Point out each malaria parasite.
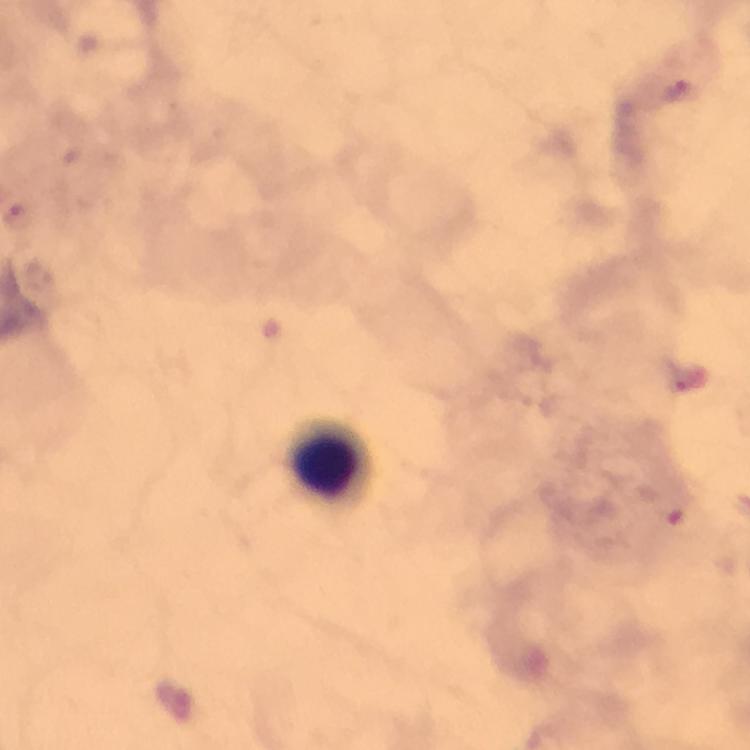

Approximate centers as [x, y] in pixels.
Malaria parasites: [694, 379].

Leukocyte locations: [325, 469]. Immersion oil was used. At 100x magnification. Image is 750×750 pixels. From a malaria diagnostic workup. Photographed with a smartphone mounted on the microscope. A crop from one field of view. Thick blood smear. Giemsa-stained preparation.